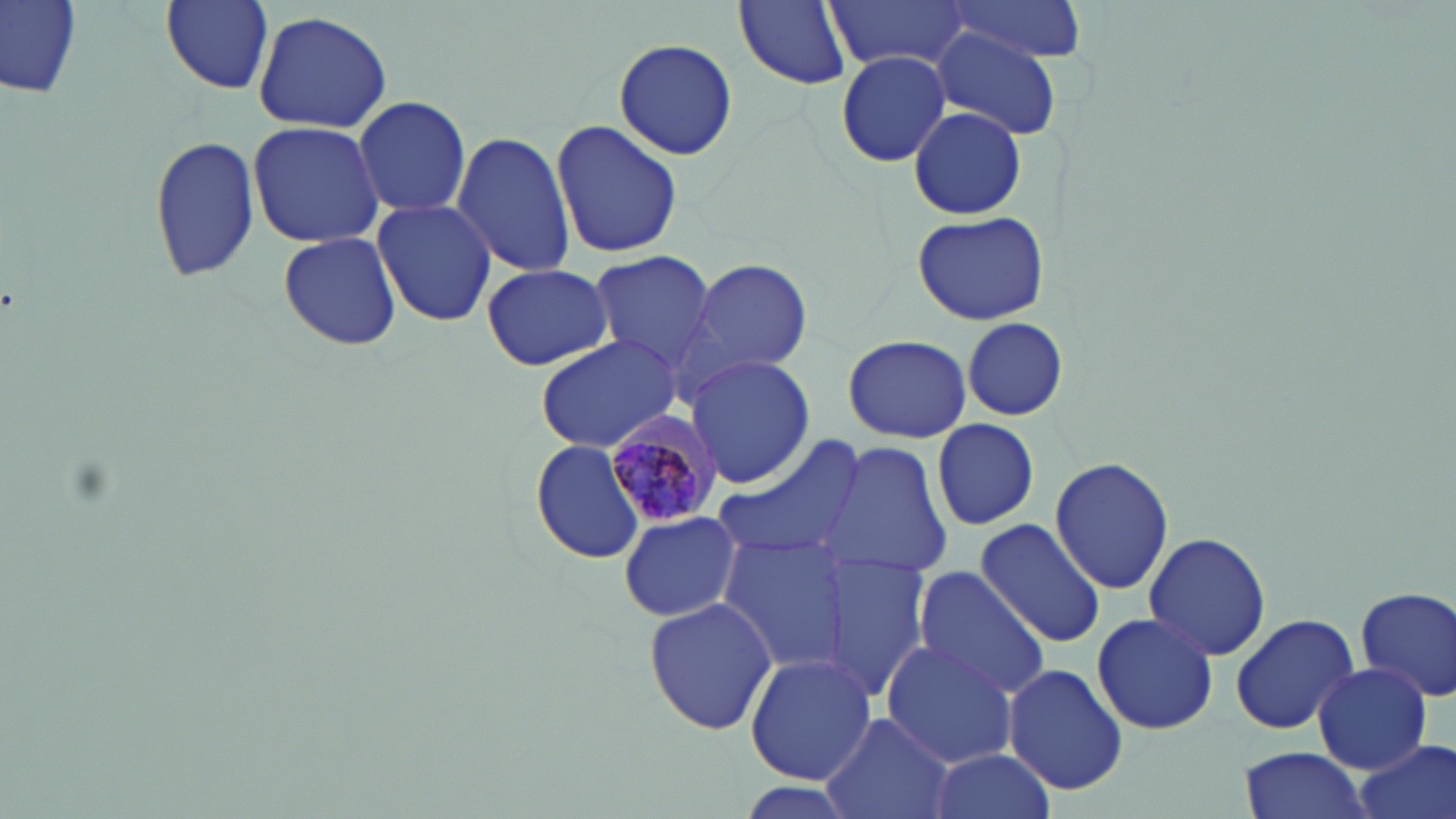
Summary:
  - Coordinate format: approximate bounding boxes as [x1, y1, x2, y2] in pixels
  - Plasmodium malariae-infected red blood cell locations: [603, 409, 722, 524]
  - Uninfected red blood cell locations: [1, 0, 83, 103], [156, 0, 274, 94], [937, 0, 1088, 63], [735, 1, 853, 88], [829, 1, 968, 70], [253, 9, 393, 134], [930, 29, 1062, 141], [613, 37, 737, 162], [835, 51, 952, 167], [352, 95, 472, 217], [909, 106, 1028, 220], [246, 120, 384, 248], [551, 121, 683, 260], [451, 130, 579, 280], [148, 133, 260, 286], [370, 197, 497, 327], [911, 211, 1051, 325], [277, 230, 403, 352], [588, 250, 720, 377], [686, 257, 812, 379], [482, 262, 613, 371], [962, 318, 1067, 419], [845, 333, 971, 442], [534, 335, 682, 457], [684, 354, 814, 490], [932, 418, 1039, 531], [712, 434, 867, 566], [531, 440, 650, 565], [823, 443, 952, 582], [1049, 458, 1173, 595], [618, 511, 741, 623], [974, 518, 1106, 648], [1143, 532, 1272, 661], [719, 533, 854, 673], [820, 548, 931, 700], [912, 568, 1053, 700], [1355, 584, 1456, 705], [643, 595, 777, 738], [1092, 610, 1219, 737], [1229, 612, 1360, 736], [880, 639, 1020, 770], [744, 653, 877, 788], [1004, 663, 1129, 795], [1314, 664, 1430, 772], [818, 712, 957, 819], [1349, 739, 1455, 819], [1240, 747, 1372, 819], [928, 749, 1056, 819]
  - Slide-level diagnosis: Plasmodium malariae
  - Image size: 1456×819 pixels
  - Field of view: single
  - Modality: light microscopy
  - Stain: May-Grünwald-Giemsa
  - Preparation: thin blood smear
  - Magnification: 1000x